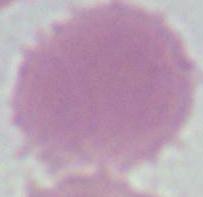
An erythrocyte is seen. Micrograph. Captured at 1000x magnification.